State which cell type is depicted.
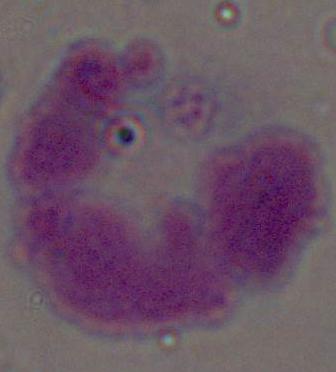
A leukocyte.

magnification = 1000x
modality = micrograph